Describe the morphology of the erythrocytes.
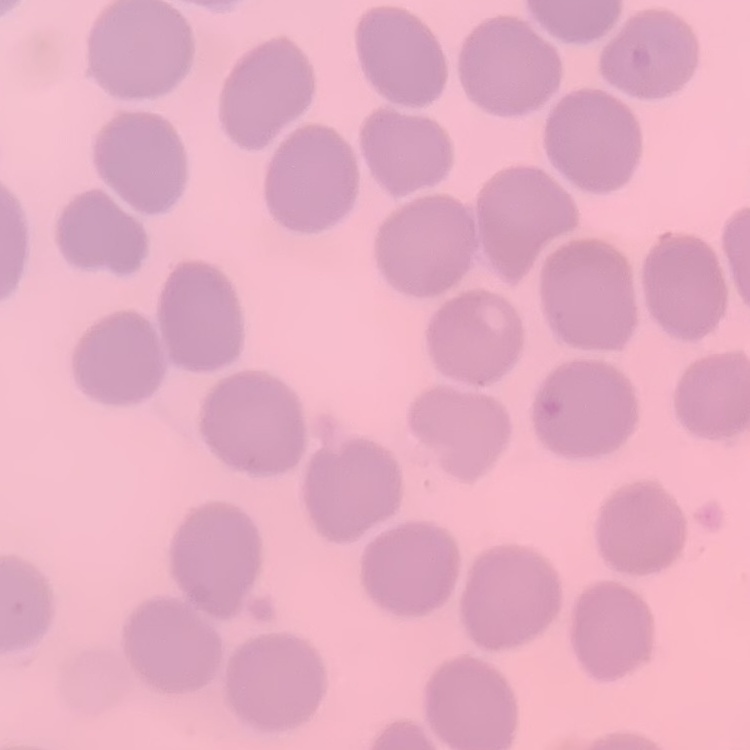
They show no rouleaux formation.

preparation = thin blood smear
image type = one tile cut from a larger photomicrograph
stain = Field's or Giemsa